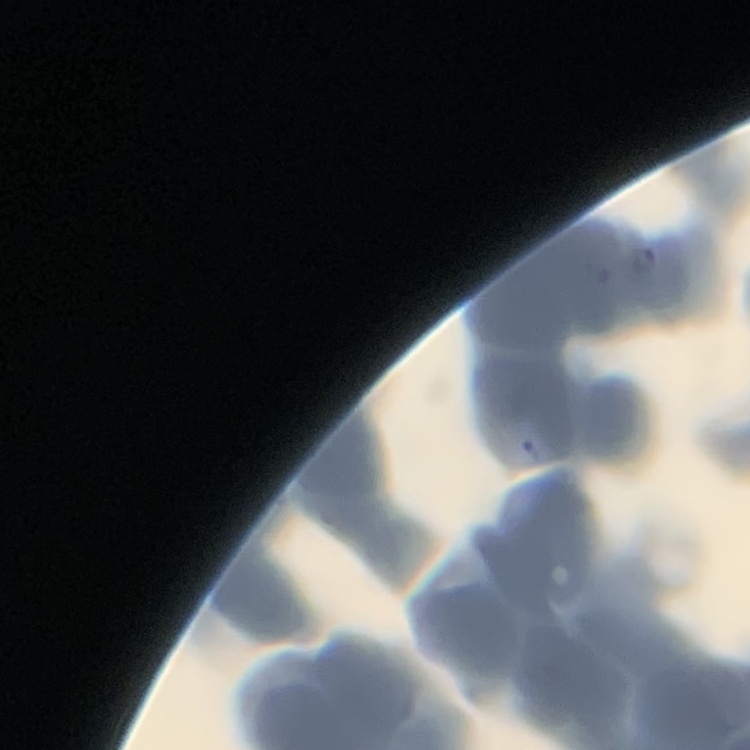
erythrocyte morphology = rouleaux formation
image type = square crop of a larger photomicrograph
stain = Field's or Giemsa
preparation = thin blood smear